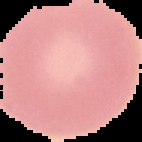

Summary:
  - Image size: 142×142 pixels
  - Image type: segmented cell region with the area outside set to black
  - Preparation: thin blood smear
  - Malaria status: uninfected